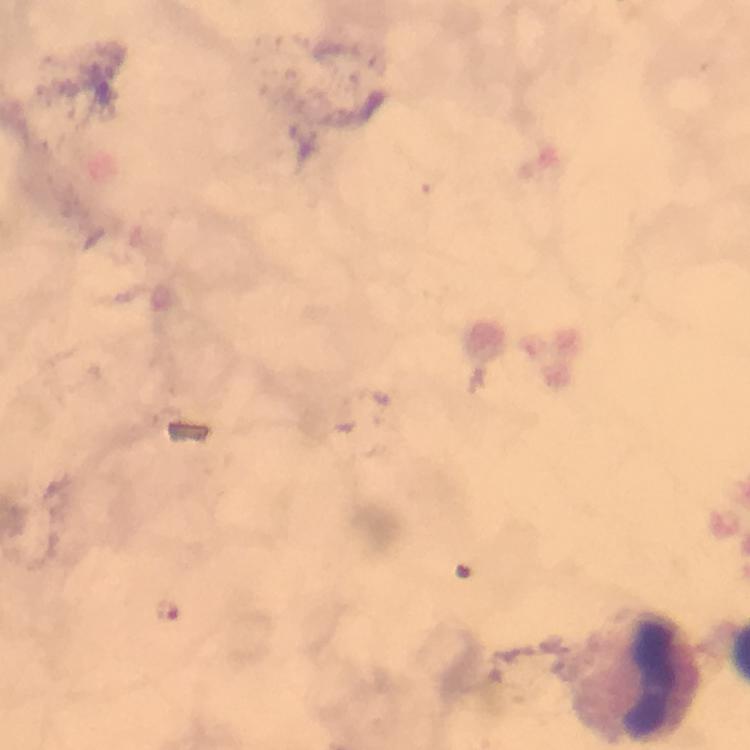

{
  "context": "from a diagnostic examination for malaria",
  "capture": "smartphone mounted on the microscope",
  "stain": "Giemsa",
  "malaria_parasite_locations": "approximate centers as (x, y) in pixels: (167, 608)",
  "immersion_oil": "used",
  "cropped_from": "one field of view",
  "preparation": "thick blood smear",
  "leukocyte_locations": "approximate centers as (x, y) in pixels: (656, 674)",
  "image_size": "750×750 pixels",
  "magnification": "100x"
}